State which parasite is depicted.
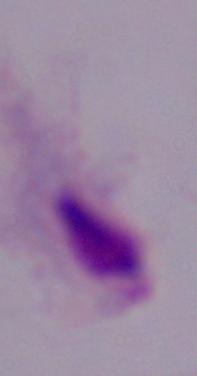

This is a trichomonad.

Photomicrograph. Captured at 1000x magnification.